Name the parasite shown.
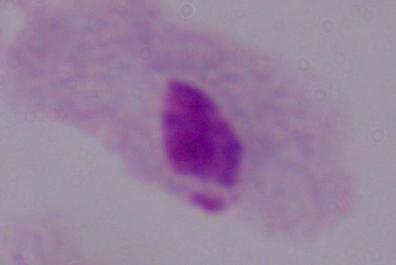

A trichomonad.

1000x magnification. Photomicrograph.